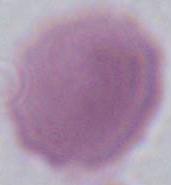
Summary:
  - Identification: erythrocyte
  - Magnification: 1000x
  - Modality: photomicrograph